Identify the preparation type.
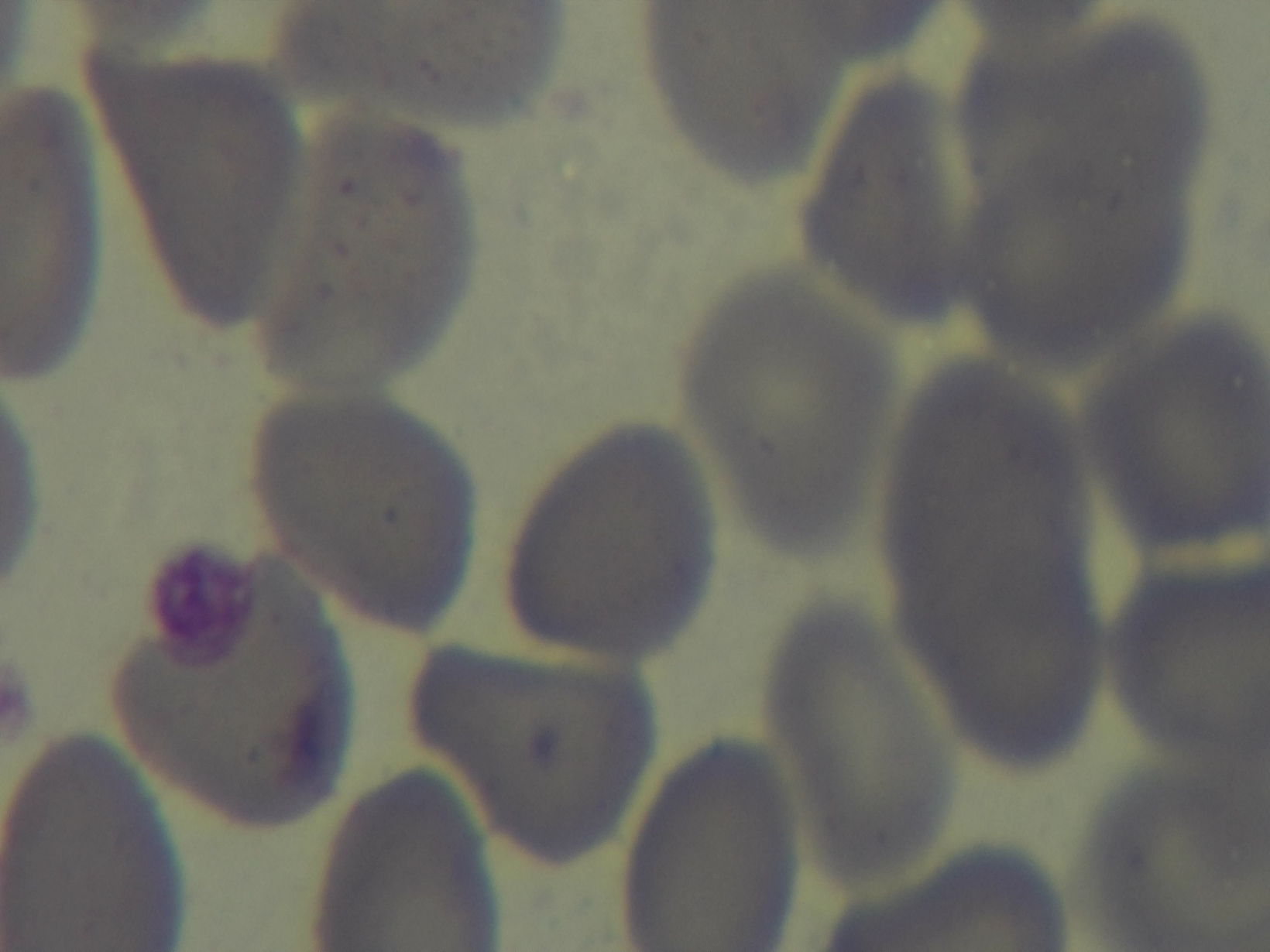
A thin smear.

Single field of view. Mounted 4K digital camera. Light microscopy. 100x oil-immersion objective. Giemsa-stained. Malaria status: uninfected.